Assess this cell for malaria.
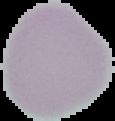
It is uninfected.

image size = 115×121 pixels
image type = cell region segmented out of the field of view; surrounding area masked to black
preparation = thin blood smear